Outline each blood parasite and name the species.
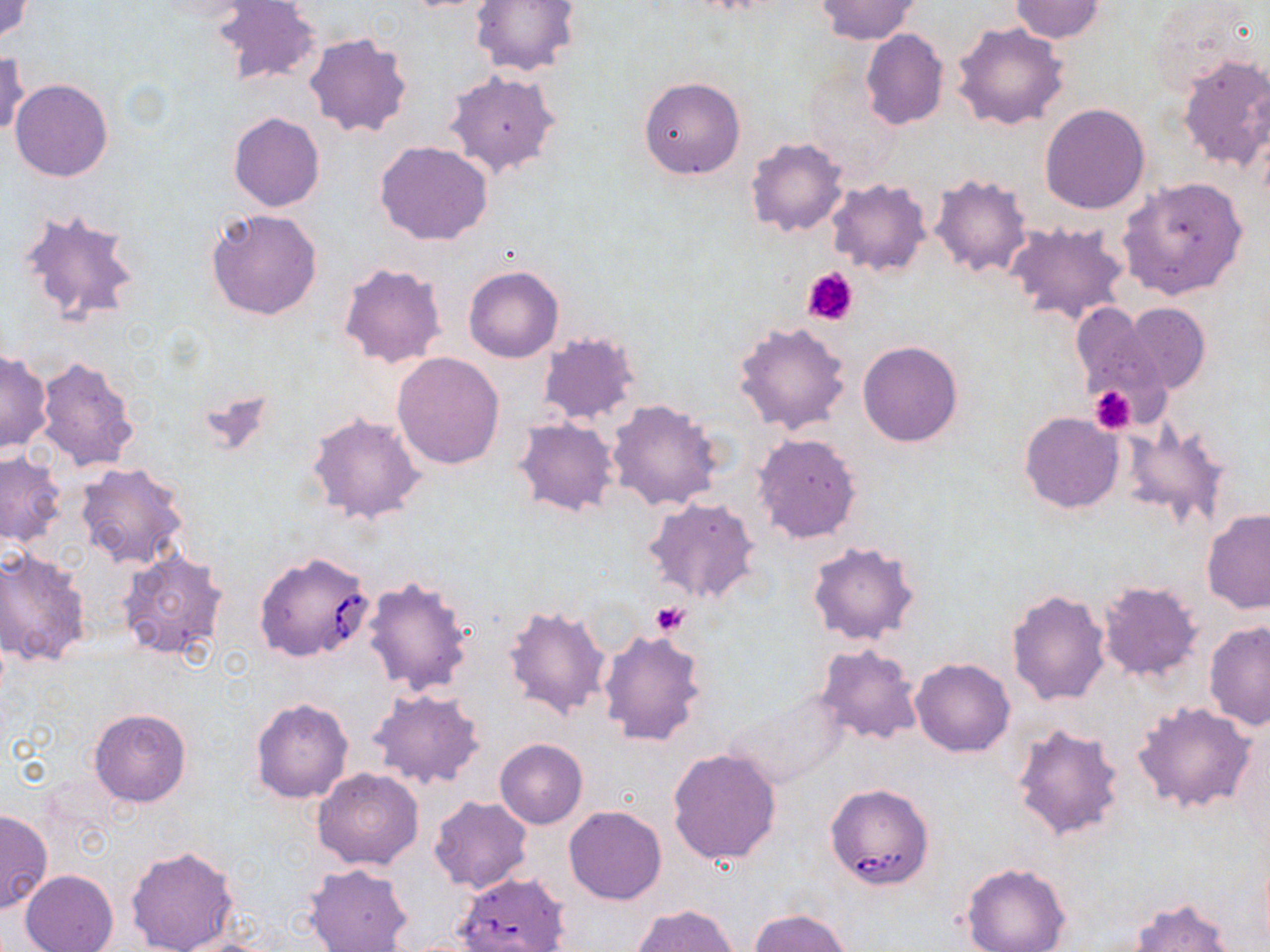
Approximate bounding boxes as named x1/y1/x2/y2 corners in pixels.
Babesia divergens-infected red blood cells: (x1=254, y1=550, x2=375, y2=662), (x1=824, y1=782, x2=934, y2=890), (x1=455, y1=871, x2=569, y2=952).
No Plasmodium falciparum, Plasmodium ovale, Plasmodium malariae, Plasmodium vivax, or Trypanosoma brucei observed.

slide_level_diagnosis: Babesia divergens
platelet_locations: 'approximate bounding boxes as named x1/y1/x2/y2 corners in pixels: (x1=803, y1=266, x2=860, y2=327), (x1=1090, y1=386, x2=1135, y2=433), (x1=650, y1=601, x2=689, y2=636)'
uninfected_red_blood_cell_locations: 'approximate bounding boxes as named x1/y1/x2/y2 corners in pixels: (x1=1, y1=0, x2=34, y2=42), (x1=470, y1=0, x2=579, y2=77), (x1=814, y1=1, x2=920, y2=43), (x1=1009, y1=1, x2=1107, y2=42), (x1=212, y1=2, x2=323, y2=87), (x1=952, y1=21, x2=1069, y2=130), (x1=860, y1=28, x2=949, y2=130), (x1=304, y1=33, x2=413, y2=140), (x1=1, y1=48, x2=29, y2=138), (x1=1175, y1=54, x2=1270, y2=174), (x1=443, y1=70, x2=562, y2=179), (x1=640, y1=77, x2=746, y2=179), (x1=10, y1=78, x2=114, y2=182), (x1=1040, y1=104, x2=1149, y2=213), (x1=229, y1=112, x2=324, y2=213), (x1=746, y1=137, x2=848, y2=238), (x1=373, y1=141, x2=494, y2=246), (x1=1117, y1=175, x2=1248, y2=301), (x1=931, y1=176, x2=1030, y2=277), (x1=827, y1=179, x2=931, y2=277), (x1=16, y1=208, x2=143, y2=331), (x1=205, y1=208, x2=323, y2=320), (x1=1004, y1=221, x2=1131, y2=327), (x1=338, y1=262, x2=447, y2=368), (x1=464, y1=266, x2=564, y2=362), (x1=1121, y1=302, x2=1210, y2=394), (x1=1070, y1=303, x2=1169, y2=412), (x1=732, y1=320, x2=853, y2=434), (x1=535, y1=332, x2=641, y2=427), (x1=858, y1=342, x2=962, y2=447), (x1=0, y1=351, x2=52, y2=454), (x1=391, y1=351, x2=505, y2=469), (x1=36, y1=357, x2=140, y2=473), (x1=194, y1=384, x2=278, y2=456), (x1=607, y1=399, x2=722, y2=511), (x1=307, y1=411, x2=427, y2=524), (x1=1020, y1=412, x2=1124, y2=514), (x1=512, y1=417, x2=619, y2=519), (x1=1122, y1=419, x2=1234, y2=531), (x1=752, y1=431, x2=863, y2=544), (x1=0, y1=451, x2=65, y2=547), (x1=75, y1=461, x2=191, y2=570), (x1=643, y1=496, x2=763, y2=607), (x1=1200, y1=509, x2=1270, y2=615), (x1=806, y1=541, x2=921, y2=647), (x1=1, y1=547, x2=90, y2=665), (x1=118, y1=548, x2=228, y2=658), (x1=361, y1=575, x2=476, y2=697), (x1=1098, y1=581, x2=1204, y2=681), (x1=1006, y1=589, x2=1110, y2=704), (x1=502, y1=604, x2=611, y2=719), (x1=1204, y1=621, x2=1270, y2=732), (x1=598, y1=628, x2=708, y2=747), (x1=812, y1=643, x2=923, y2=747), (x1=910, y1=657, x2=1015, y2=757), (x1=366, y1=687, x2=485, y2=791), (x1=718, y1=688, x2=852, y2=793), (x1=251, y1=697, x2=354, y2=804), (x1=1130, y1=700, x2=1258, y2=812), (x1=89, y1=708, x2=191, y2=807), (x1=1010, y1=721, x2=1127, y2=844), (x1=495, y1=739, x2=588, y2=828), (x1=668, y1=747, x2=781, y2=863), (x1=313, y1=767, x2=424, y2=870), (x1=429, y1=797, x2=531, y2=894), (x1=563, y1=806, x2=667, y2=904), (x1=0, y1=810, x2=52, y2=914), (x1=125, y1=845, x2=241, y2=952), (x1=959, y1=862, x2=1071, y2=952), (x1=305, y1=863, x2=413, y2=952), (x1=20, y1=869, x2=119, y2=952), (x1=1129, y1=896, x2=1238, y2=952), (x1=631, y1=904, x2=739, y2=952), (x1=750, y1=909, x2=851, y2=952), (x1=173, y1=937, x2=281, y2=952)'
stain: May-Grünwald-Giemsa
modality: light microscopy
preparation: thin blood film
image_size: 1270×952 pixels
field_of_view: single
magnification: 1000x